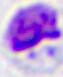

A leukocyte is seen. Photomicrograph. Captured at 400x magnification.